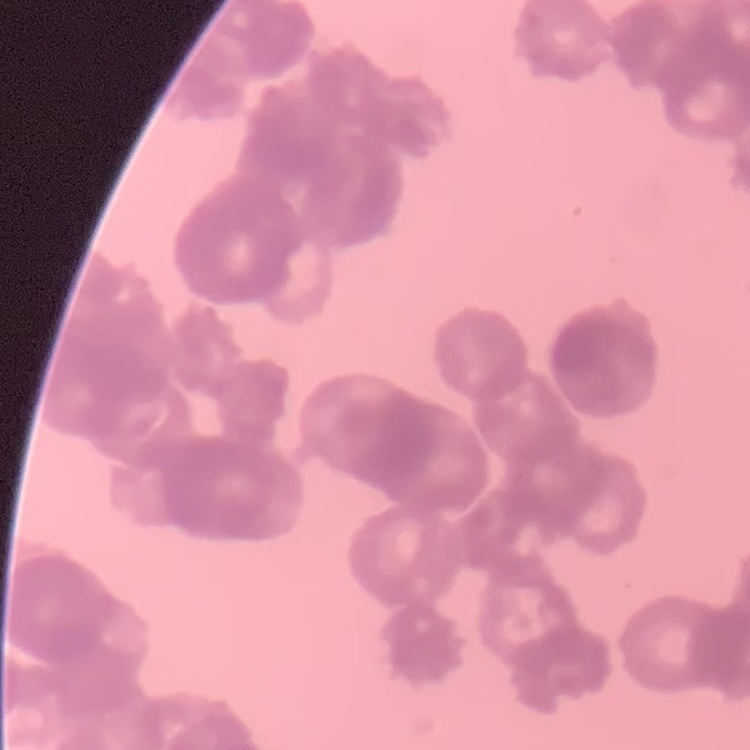
Summary:
  - Red blood cell morphology: rouleaux formation
  - Preparation: thin peripheral smear
  - Image type: square crop of a larger photomicrograph
  - Stain: Field's or Giemsa